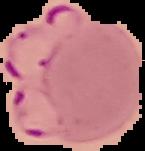

Summary:
  - Image type: segmented cell region on a black background
  - Preparation: thin blood film
  - Result: Plasmodium parasites identified
  - Image size: 145×151 pixels